Locate every Plasmodium parasite.
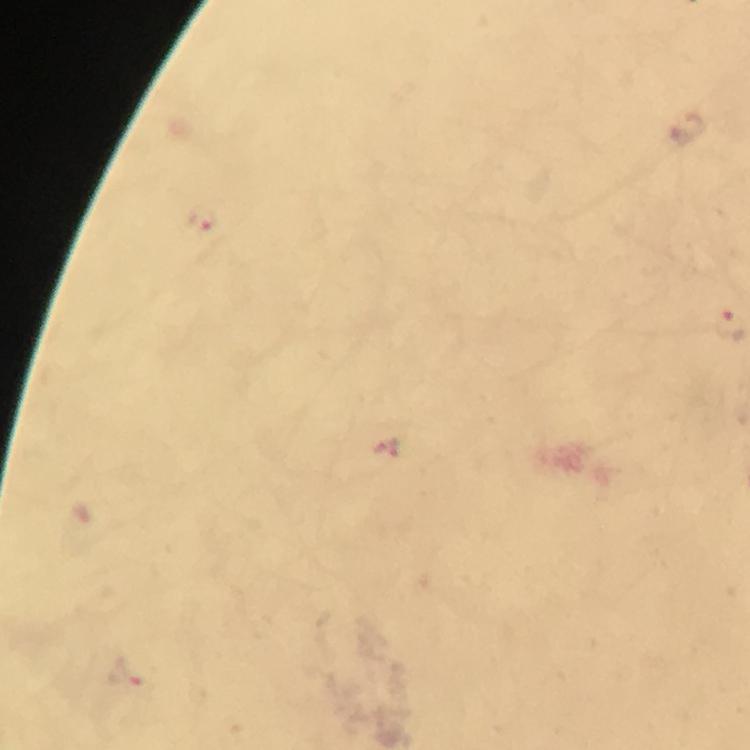

Approximate centers as (x, y) in pixels.
Plasmodium parasites: (205, 220), (128, 673).

immersion_oil: used
stain: Giemsa
capture: smartphone camera through the microscope
cropped_from: a single field of view
image_size: 750×750 pixels
preparation: thick blood smear
context: from a malaria diagnostic workup
magnification: 100x